Assess the morphology of the red blood cells.
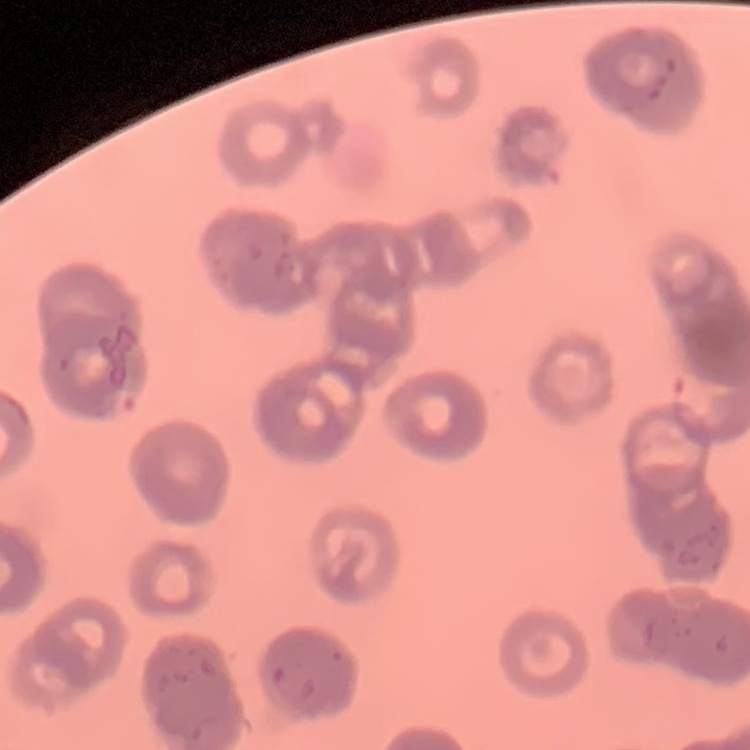

They show rouleaux formation.

Summary:
  - Stain: Field's or Giemsa
  - Preparation: thin blood film
  - Image type: square crop of a larger photomicrograph